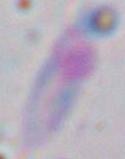

Summary:
  - Identification: Toxoplasma gondii
  - Magnification: 1000x
  - Modality: photomicrograph